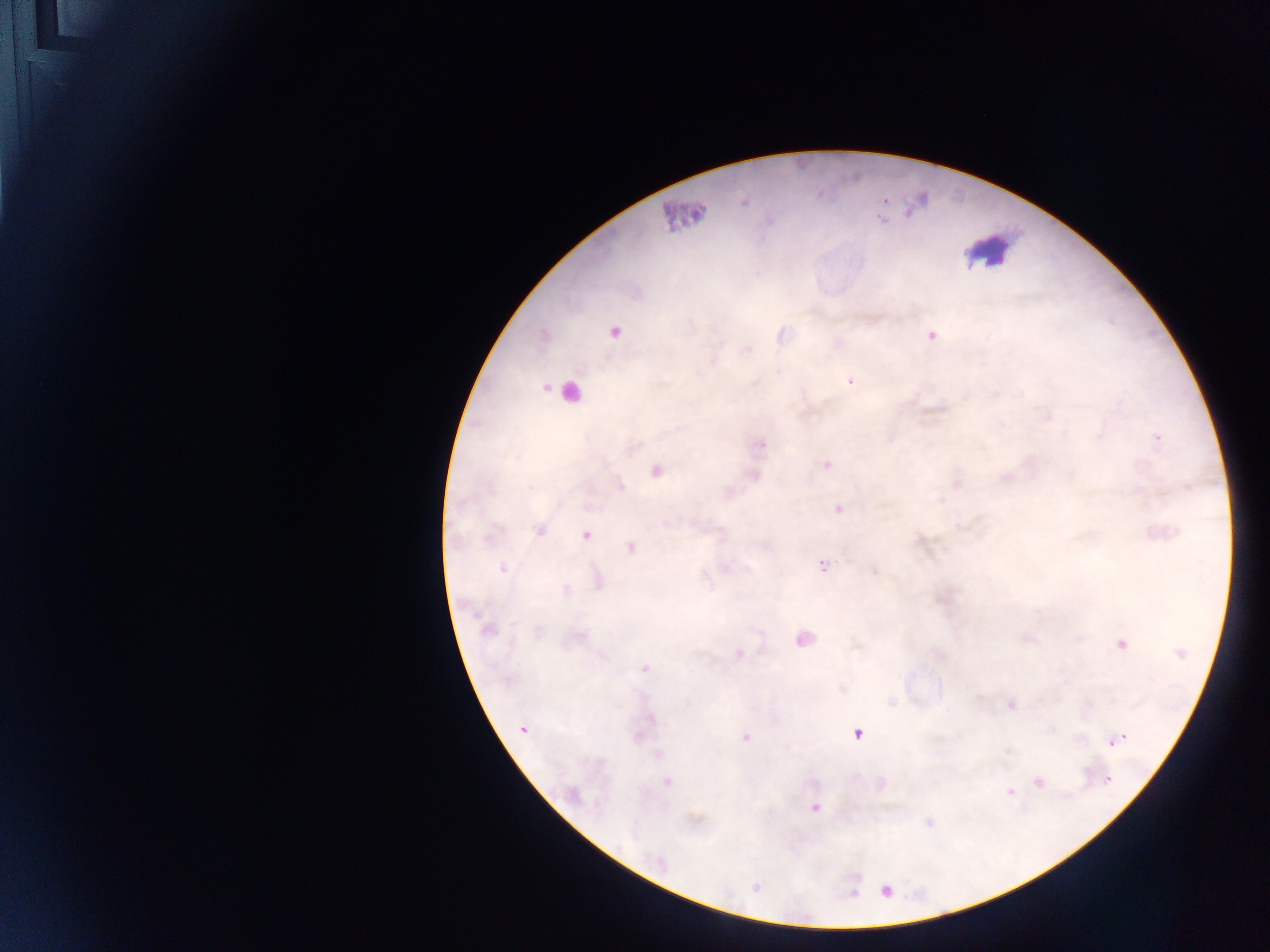

Approximate centers as x y in pixels.
Summary:
  - Leukocyte locations: 986 252
  - Plasmodium parasite locations: 743 200; 884 201; 695 212; 688 215; 882 219; 613 331; 781 335; 930 336; 838 343; 850 380; 1047 415; 1156 438; 760 446; 826 464; 655 471; 753 475; 1005 478; 957 482; 620 487; 838 509; 959 526; 538 530; 585 534; 630 546; 821 564; 502 568; 875 571; 597 581; 566 591; 487 629; 577 637; 804 638; 1121 644; 739 654; 644 669; 1011 704; 523 728; 857 733; 1122 737; 745 738; 1115 740; 1108 741; 1007 750; 657 754; 1107 779; 666 781; 1037 781; 1010 791; 813 807; 929 821; 657 861; 755 887; 886 891
  - Object labeled both Plasmodium parasite and leukocyte by the source: 569 391
  - Image size: 1270×952 pixels
  - Country: Ghana
  - Field of view: single
  - Preparation: thick blood film
  - Capture: mobile-phone photograph through a microscope